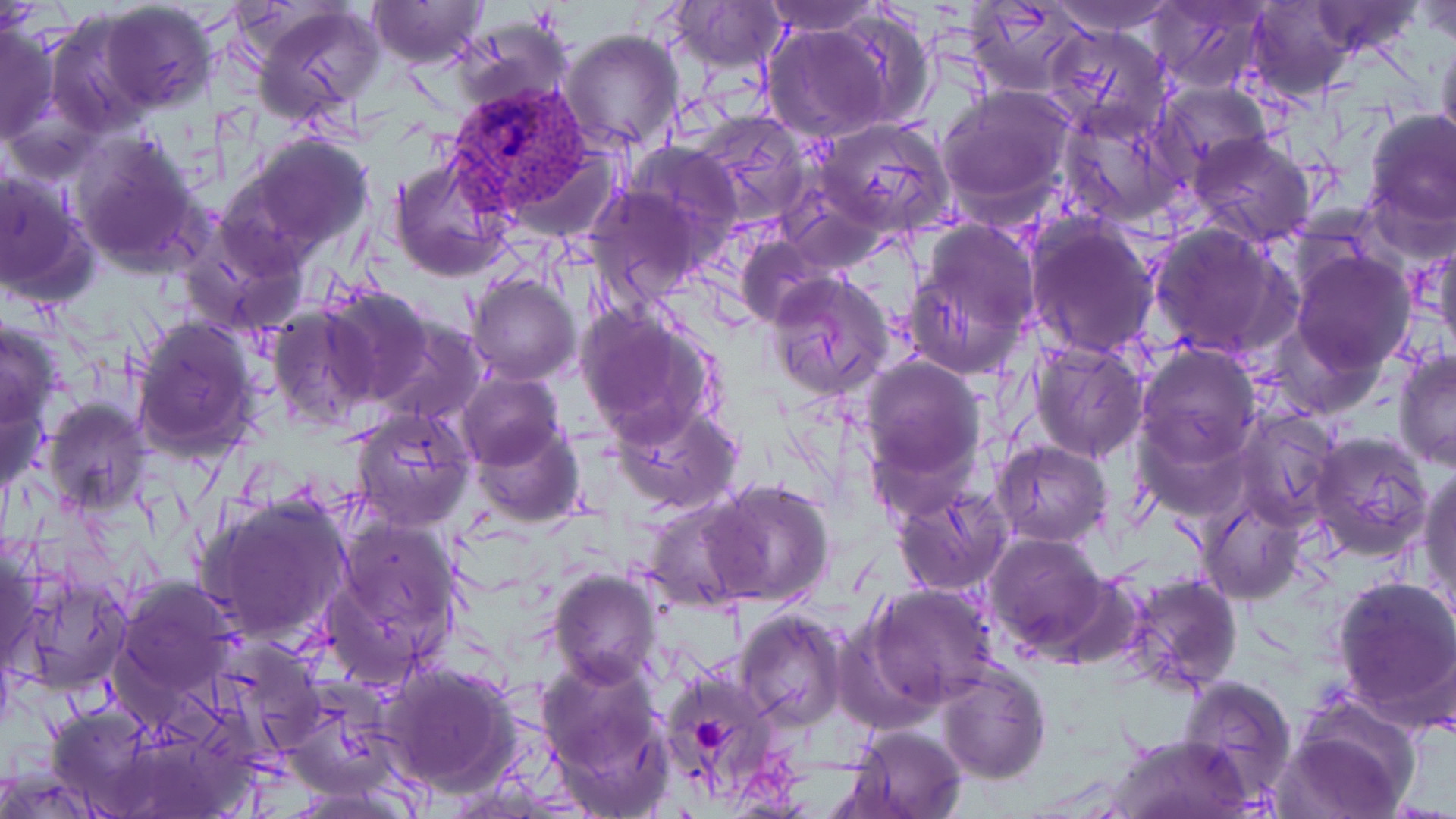 Approximate bounding boxes as (x1,y1)-(x2,y2) corner pairs in pixels. Uninfected red blood cell locations: (366,0)-(489,70), (758,0)-(884,35), (965,0)-(1091,95), (1044,0)-(1185,34), (1146,0)-(1271,93), (98,1)-(216,113), (665,2)-(786,73), (1305,2)-(1426,57), (1414,2)-(1455,48), (248,3)-(387,126), (1242,3)-(1358,101), (826,8)-(936,131), (41,14)-(150,133), (450,18)-(574,120), (0,22)-(59,145), (762,23)-(890,144), (1043,24)-(1175,142), (1435,29)-(1456,159), (559,30)-(687,154), (1154,80)-(1273,181), (937,87)-(1076,216), (1059,106)-(1192,227), (1361,108)-(1455,231), (689,116)-(815,227), (817,118)-(955,237), (1186,131)-(1320,247), (70,134)-(207,273), (246,134)-(372,253), (624,141)-(741,248), (388,156)-(517,280), (1,167)-(94,305), (584,180)-(711,307), (903,219)-(1042,380), (1024,219)-(1163,359), (179,221)-(306,339), (1147,221)-(1296,359), (1430,234)-(1456,363), (735,235)-(837,329), (1287,248)-(1417,374), (765,271)-(897,402), (466,274)-(580,385), (319,283)-(439,406), (266,302)-(381,431), (576,306)-(720,444), (367,314)-(488,426), (0,315)-(63,432), (129,316)-(262,461), (1029,341)-(1147,462), (1135,343)-(1261,467), (1393,348)-(1456,471), (859,356)-(984,486), (457,371)-(567,473), (0,387)-(51,494), (42,399)-(150,515), (612,400)-(744,514), (350,407)-(477,530), (1233,412)-(1340,529), (1131,416)-(1249,522), (471,417)-(584,529), (1309,432)-(1433,560), (992,439)-(1112,549), (1420,463)-(1456,614), (705,477)-(835,605), (892,487)-(1011,596), (197,492)-(355,647), (640,495)-(758,611), (1198,495)-(1304,605), (324,515)-(463,685), (983,532)-(1112,657), (0,540)-(45,677), (14,566)-(131,698), (549,566)-(665,689), (1116,573)-(1244,697), (1331,576)-(1456,721), (113,577)-(242,704), (868,584)-(1002,707), (733,608)-(847,730), (536,656)-(676,809), (377,661)-(517,795), (657,665)-(780,802), (937,665)-(1050,784), (1177,674)-(1298,803), (1284,697)-(1422,816), (44,703)-(161,816), (842,723)-(968,819), (1111,733)-(1250,818). Plasmodium vivax-infected red blood cell locations: (446,81)-(599,219). Platelet locations: (693,716)-(731,757). Slide-level diagnosis: Plasmodium vivax. Single field of view. Thin blood smear. Image is 1456×819 pixels. May-Grünwald-Giemsa-stained preparation. Optical microscopy. Captured at 1000x magnification.